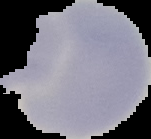
{
  "image_size": "151×139 pixels",
  "preparation": "thin blood film",
  "malaria_status": "uninfected",
  "image_type": "segmented cell region with the area outside set to black"
}